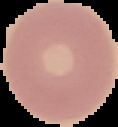 Image is 118×127 pixels. Malaria status: uninfected. Cell region segmented out of the field of view; the surrounding area is masked to black. From a thin blood film.